Classify this cell by malaria status.
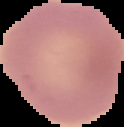

Uninfected.

The area outside the segmented cell region is set to black. From a thin blood smear. Image is 124×127 pixels.